State which parasite is depicted.
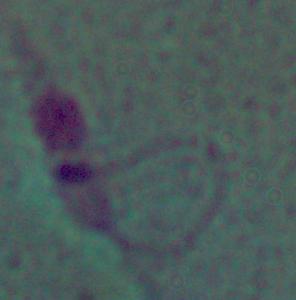
This is Leishmania.

Photomicrograph. 1000x magnification.